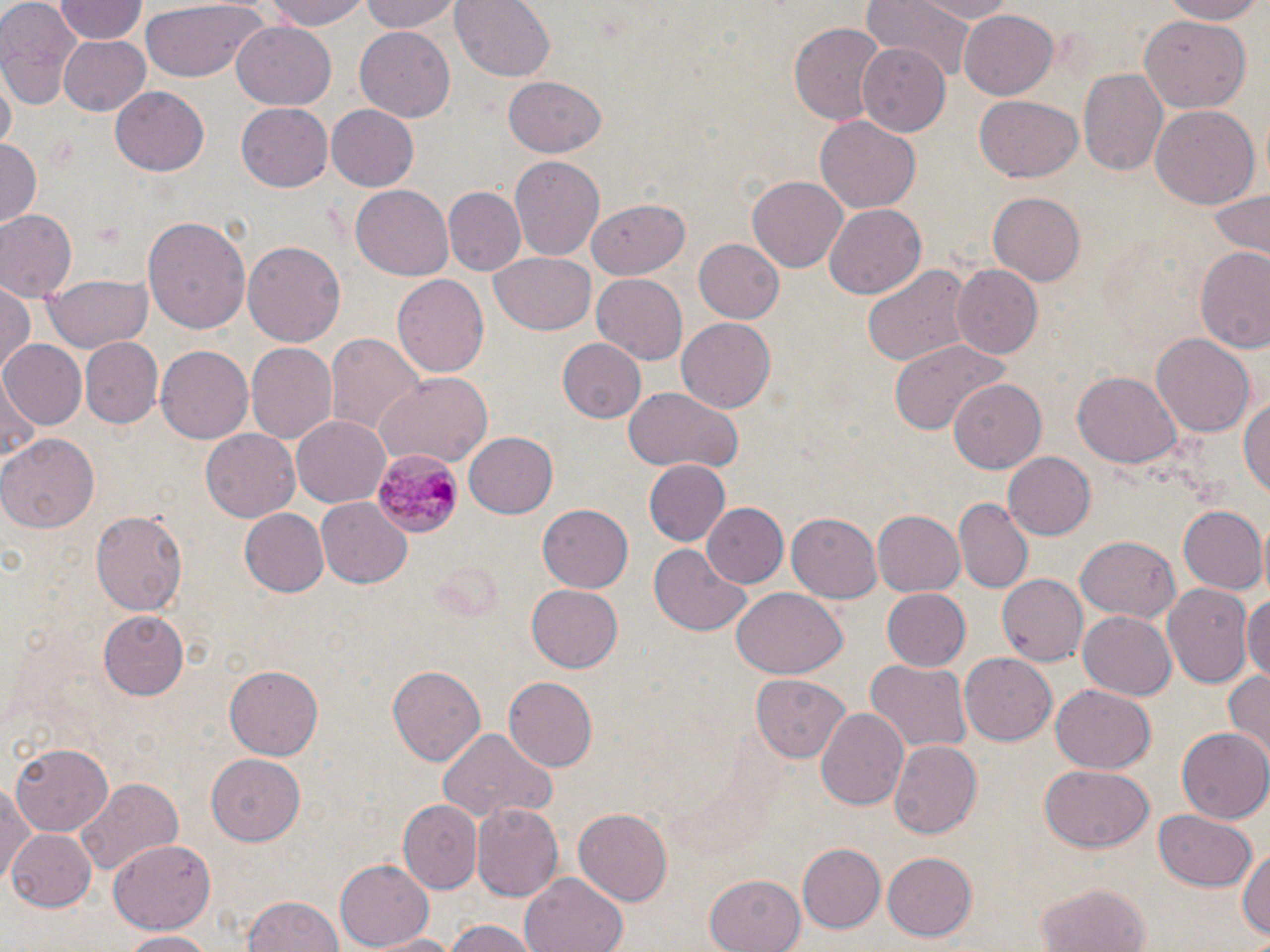

slide_level_diagnosis: Plasmodium malariae
image_size: 1270×952 pixels
plasmodium_malariae_infected_red_blood_cell_locations: 'approximate bounding boxes as (x1, y1, x2, y2) in pixels: (372, 449, 461, 538)'
preparation: thin blood smear
magnification: 1000x
field_of_view: one of a larger specimen
uninfected_red_blood_cell_locations: 'approximate bounding boxes as (x1, y1, x2, y2) in pixels: (0, 0, 84, 106), (54, 0, 147, 43), (269, 0, 370, 31), (357, 0, 460, 34), (450, 0, 555, 80), (909, 0, 1022, 22), (1159, 0, 1270, 24), (860, 1, 985, 78), (136, 2, 264, 82), (63, 3, 146, 89), (958, 8, 1058, 100), (1140, 17, 1253, 112), (232, 20, 337, 109), (789, 20, 886, 128), (354, 27, 455, 122), (57, 34, 152, 117), (859, 42, 951, 136), (1078, 69, 1166, 179), (501, 75, 606, 158), (110, 85, 210, 176), (974, 96, 1087, 182), (235, 104, 333, 192), (327, 104, 419, 190), (1150, 105, 1259, 212), (815, 116, 920, 213), (0, 138, 40, 225), (509, 156, 605, 261), (747, 173, 849, 271), (351, 185, 453, 281), (442, 186, 525, 277), (1204, 187, 1270, 258), (987, 190, 1090, 286), (588, 196, 691, 280), (824, 203, 928, 300), (0, 208, 79, 301), (143, 216, 250, 332), (692, 238, 784, 323), (243, 239, 345, 349), (1196, 245, 1270, 356), (489, 252, 596, 336), (859, 262, 972, 371), (952, 264, 1042, 358), (44, 273, 152, 353), (592, 273, 688, 363), (393, 274, 490, 379), (0, 285, 34, 376), (675, 314, 776, 410), (1151, 331, 1254, 436), (326, 332, 424, 438), (80, 337, 162, 427), (556, 337, 646, 424), (890, 338, 1002, 440), (0, 341, 85, 430), (246, 343, 338, 445), (156, 346, 252, 444), (1074, 369, 1180, 468), (375, 372, 493, 466), (0, 377, 39, 470), (948, 380, 1045, 474), (1242, 387, 1270, 504), (623, 388, 742, 473), (291, 414, 391, 505), (200, 428, 300, 523), (464, 430, 558, 519), (1, 432, 96, 532), (1003, 450, 1096, 540), (644, 460, 731, 547), (316, 497, 413, 588), (955, 499, 1032, 592), (702, 502, 788, 587), (537, 503, 634, 592), (1179, 504, 1269, 594), (239, 509, 330, 597), (873, 510, 965, 596), (92, 511, 186, 618), (787, 512, 882, 601), (1076, 536, 1180, 626), (648, 544, 751, 636), (996, 574, 1087, 665), (1162, 582, 1254, 688), (526, 583, 622, 673), (730, 588, 846, 679), (880, 588, 971, 671), (1245, 590, 1270, 689), (1078, 608, 1178, 700), (100, 610, 192, 701), (960, 650, 1057, 743), (864, 659, 972, 755), (224, 664, 324, 758), (388, 664, 485, 764), (1226, 668, 1270, 760), (751, 674, 850, 761), (502, 678, 596, 772), (1050, 684, 1154, 773), (816, 706, 910, 812), (436, 728, 556, 824), (1176, 728, 1269, 821), (889, 741, 981, 839), (9, 744, 114, 836), (207, 753, 304, 848), (1040, 765, 1153, 852), (75, 778, 180, 873), (1, 783, 32, 884), (398, 798, 481, 893), (470, 802, 562, 903), (574, 808, 675, 905), (1152, 809, 1259, 892), (9, 829, 98, 910), (107, 837, 216, 934), (798, 843, 887, 933), (1238, 846, 1270, 944), (882, 850, 977, 942), (334, 857, 434, 949), (521, 872, 627, 952), (704, 873, 807, 952), (1034, 880, 1155, 952), (243, 894, 345, 952), (441, 918, 541, 952), (117, 931, 222, 950), (365, 931, 461, 951)'
stain: May-Grünwald-Giemsa
modality: optical microscopy